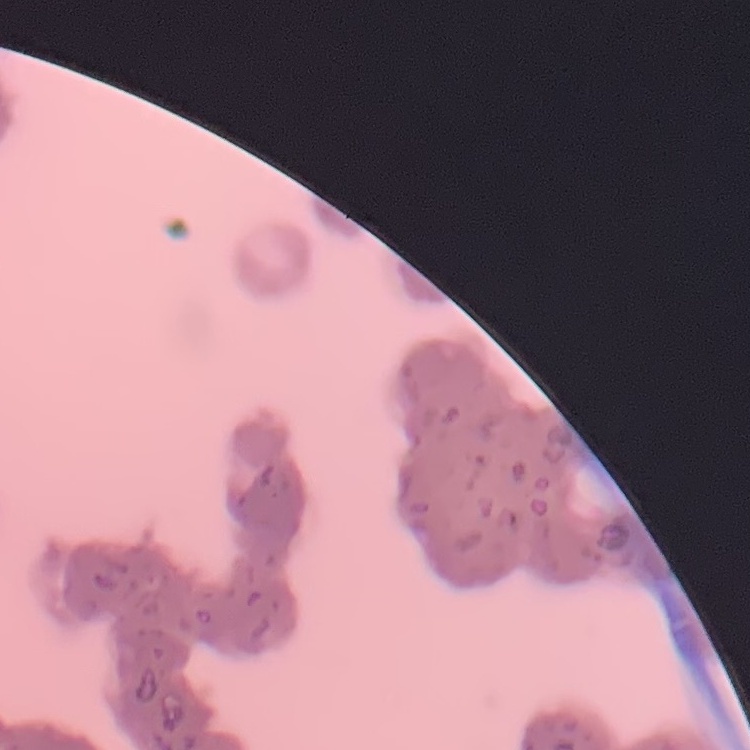

Summary:
  - Erythrocyte morphology: rouleaux formation
  - Image type: one tile cut from a larger photomicrograph
  - Stain: Field's or Giemsa
  - Preparation: thin peripheral smear